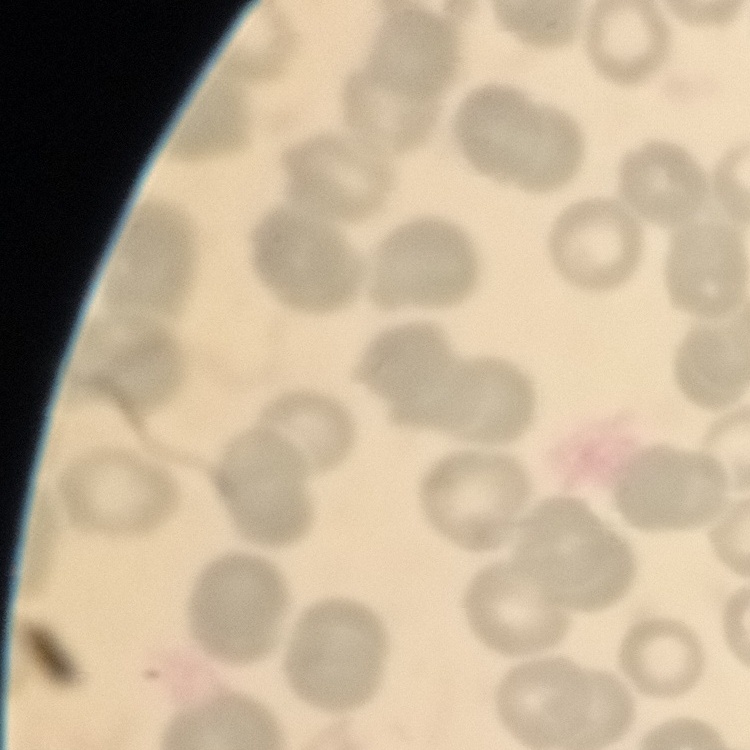
The red blood cells exhibit no rouleaux formation. Thin blood film. Square crop of a larger photomicrograph. Field's or Giemsa stain.